Assess this cell for malaria.
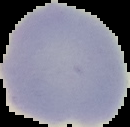
It is uninfected.

preparation: thin blood smear
image_type: cell region segmented out of the field of view; surrounding area masked to black
image_size: 130×127 pixels